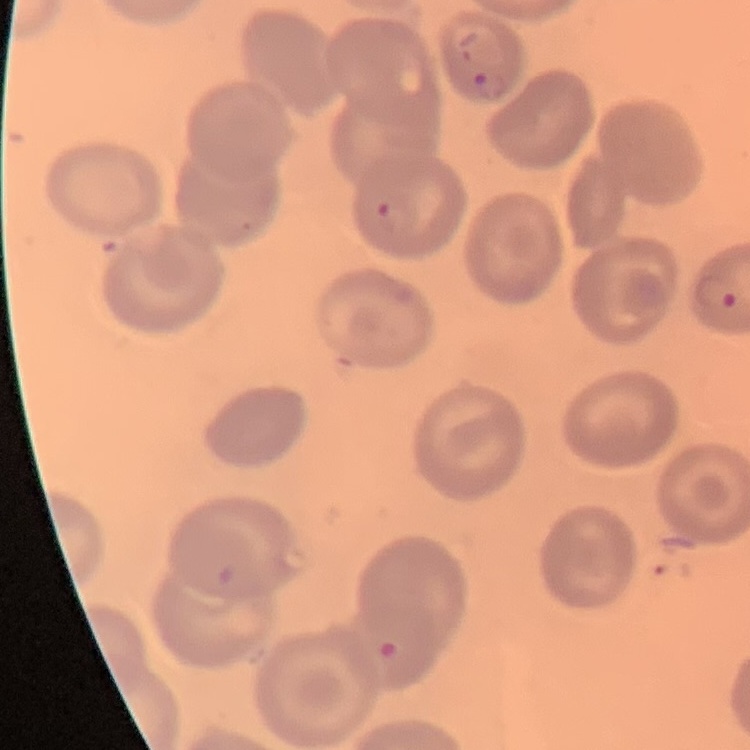 The erythrocytes exhibit no rouleaux formation. One tile cut from a larger photomicrograph. Thin blood film. Stained with either Field's or Giemsa.